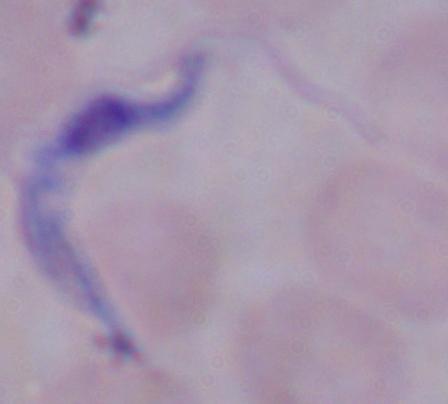
1000x magnification. A trypanosome is shown. Photomicrograph.